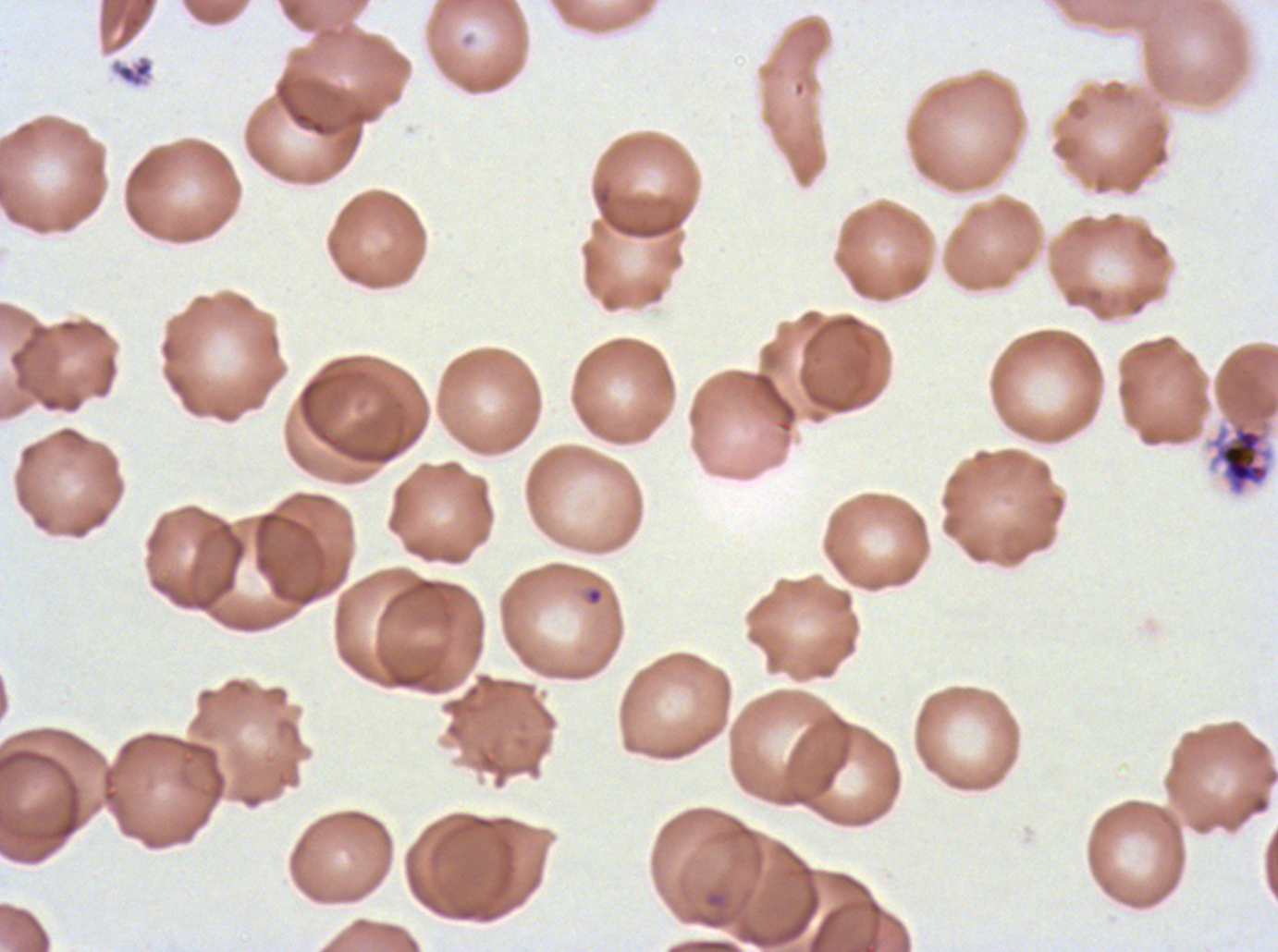

Approximate bounding boxes as [x1, y1, x2, y2] in pixels. Debris locations: [109, 55, 154, 89]. Segmenter locations: [1210, 421, 1272, 495]. Giemsa-stained preparation. Ex-vivo P. falciparum culture from a patient in The Gambia, grown for 24 to 48 hours. Thin blood smear. Image is 1278×952 pixels. A sub-image separated from a larger composite.